Outline each blood parasite and name the species.
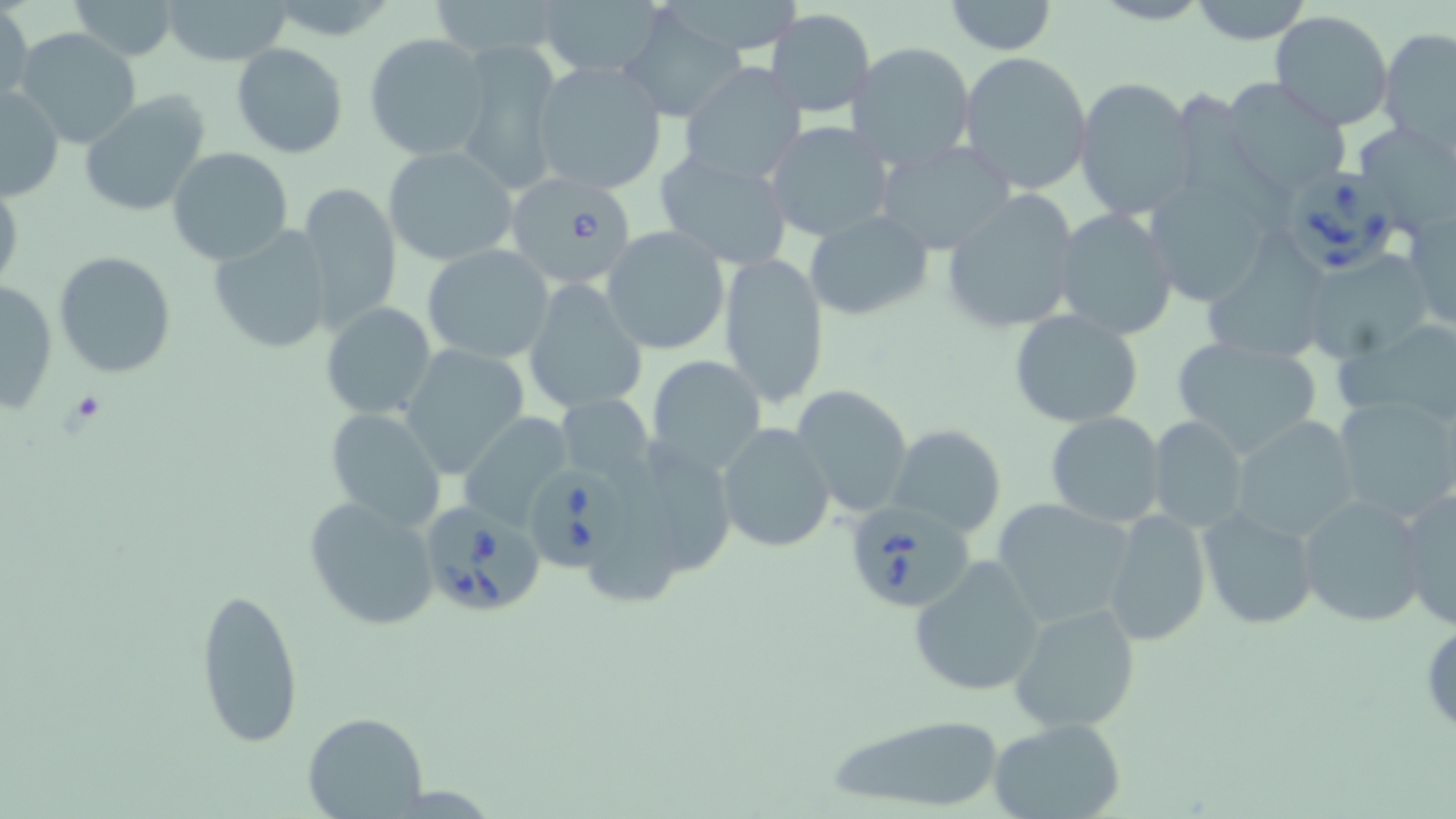
Approximate bounding boxes as (x1,y1)-(x2,y2) corner pairs in pixels.
Babesia divergens-infected red blood cells: (514,177)-(645,285), (1284,177)-(1397,278), (527,466)-(629,572), (855,498)-(979,606), (418,502)-(548,620).
No Plasmodium falciparum, Plasmodium ovale, Plasmodium malariae, Plasmodium vivax, or Trypanosoma brucei observed.

slide-level diagnosis = Babesia divergens
stain = May-Grünwald-Giemsa
magnification = 1000x
platelet locations = approximate bounding boxes as (x1,y1)-(x2,y2) corner pairs in pixels: (66,389)-(109,428)
field of view = one of a larger specimen
image size = 1456×819 pixels
uninfected red blood cell locations = approximate bounding boxes as (x1,y1)-(x2,y2) corner pairs in pixels: (66,0)-(183,61), (160,0)-(296,67), (942,0)-(1059,54), (1187,0)-(1316,45), (436,1)-(566,53), (535,1)-(663,79), (1,4)-(33,111), (618,7)-(745,122), (765,8)-(875,119), (1269,12)-(1397,131), (15,28)-(141,149), (1378,29)-(1456,152), (364,33)-(490,161), (455,37)-(563,192), (846,42)-(977,172), (230,43)-(348,159), (958,51)-(1093,195), (531,60)-(668,198), (678,63)-(808,186), (1073,76)-(1199,220), (1222,78)-(1352,195), (0,86)-(65,200), (1155,87)-(1270,303), (80,88)-(215,218), (763,121)-(894,243), (1361,129)-(1456,240), (873,140)-(1020,256), (382,145)-(518,267), (167,147)-(293,264), (652,148)-(795,271), (0,178)-(24,301), (294,180)-(403,333), (938,190)-(1083,335), (1051,208)-(1178,341), (1404,211)-(1456,334), (804,212)-(933,321), (207,225)-(335,355), (601,225)-(731,355), (1203,241)-(1333,364), (421,243)-(557,366), (718,251)-(830,408), (1303,251)-(1435,364), (54,252)-(177,376), (523,277)-(649,417), (1,281)-(58,416), (320,302)-(436,420), (1008,309)-(1143,426), (1338,319)-(1456,426), (1172,333)-(1324,457), (399,344)-(531,479), (646,354)-(768,477), (672,372)-(805,528), (790,384)-(914,518), (1331,393)-(1456,523), (557,394)-(653,488), (326,408)-(448,529), (458,409)-(578,529), (1045,411)-(1166,527), (1147,415)-(1250,533), (1229,416)-(1364,543), (716,422)-(836,553), (888,424)-(1006,537), (1394,485)-(1456,634), (1299,494)-(1431,627), (303,496)-(440,632), (991,497)-(1136,630), (1100,508)-(1213,647), (1197,508)-(1320,632), (906,556)-(1047,698), (193,583)-(305,751), (1009,601)-(1140,733), (1419,615)-(1456,738), (303,712)-(427,819), (818,713)-(1012,814), (987,718)-(1128,819)
modality = optical microscopy
preparation = thin blood smear